Describe the morphology of the red blood cells.
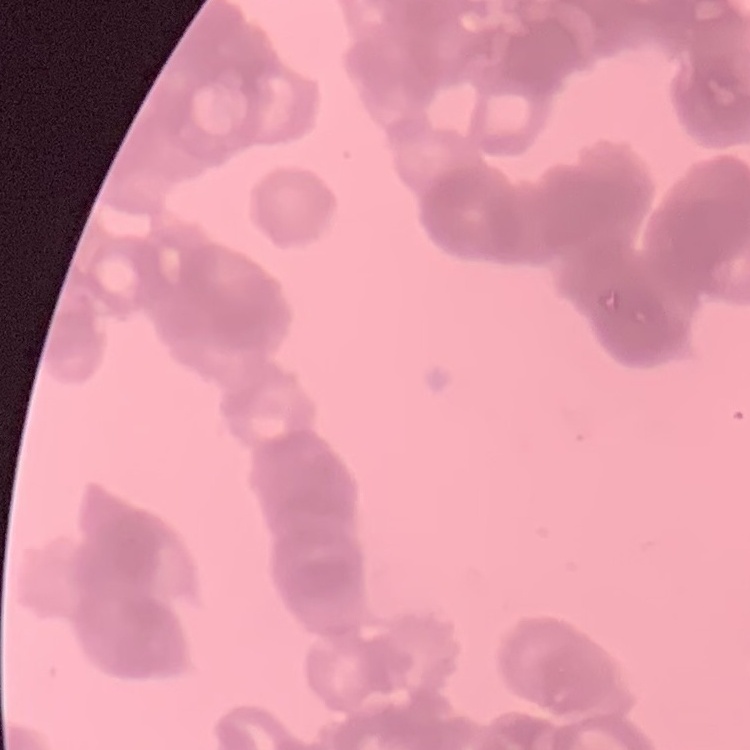

They show rouleaux formation.

Field's or Giemsa stain. Thin peripheral smear. Square crop of a larger photomicrograph.